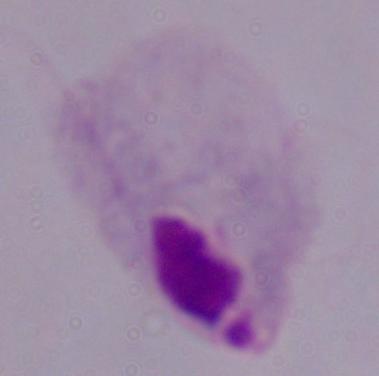
A trichomonad is seen. Captured at 1000x magnification. Micrograph.